Identify the parasite.
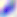

This is Toxoplasma gondii.

Captured at 400x magnification. Micrograph.